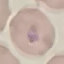
Result: malaria parasites detected. Acquired by smartphone through the microscope eyepiece. Cell patch, automatically extracted from a larger field of view and resized to 64 × 64 pixels. Giemsa stain. Thin blood smear.